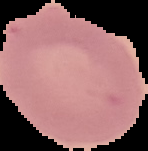

Summary:
  - Image size: 148×151 pixels
  - Malaria status: uninfected
  - Preparation: thin blood smear
  - Image type: segmented cell region on a black background